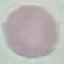
Malaria status: uninfected. Photographed with a smartphone camera at the microscope eyepiece. Thin blood smear. Giemsa-stained preparation. Cell patch, automatically extracted from a larger field of view and resized to 64 × 64 pixels.